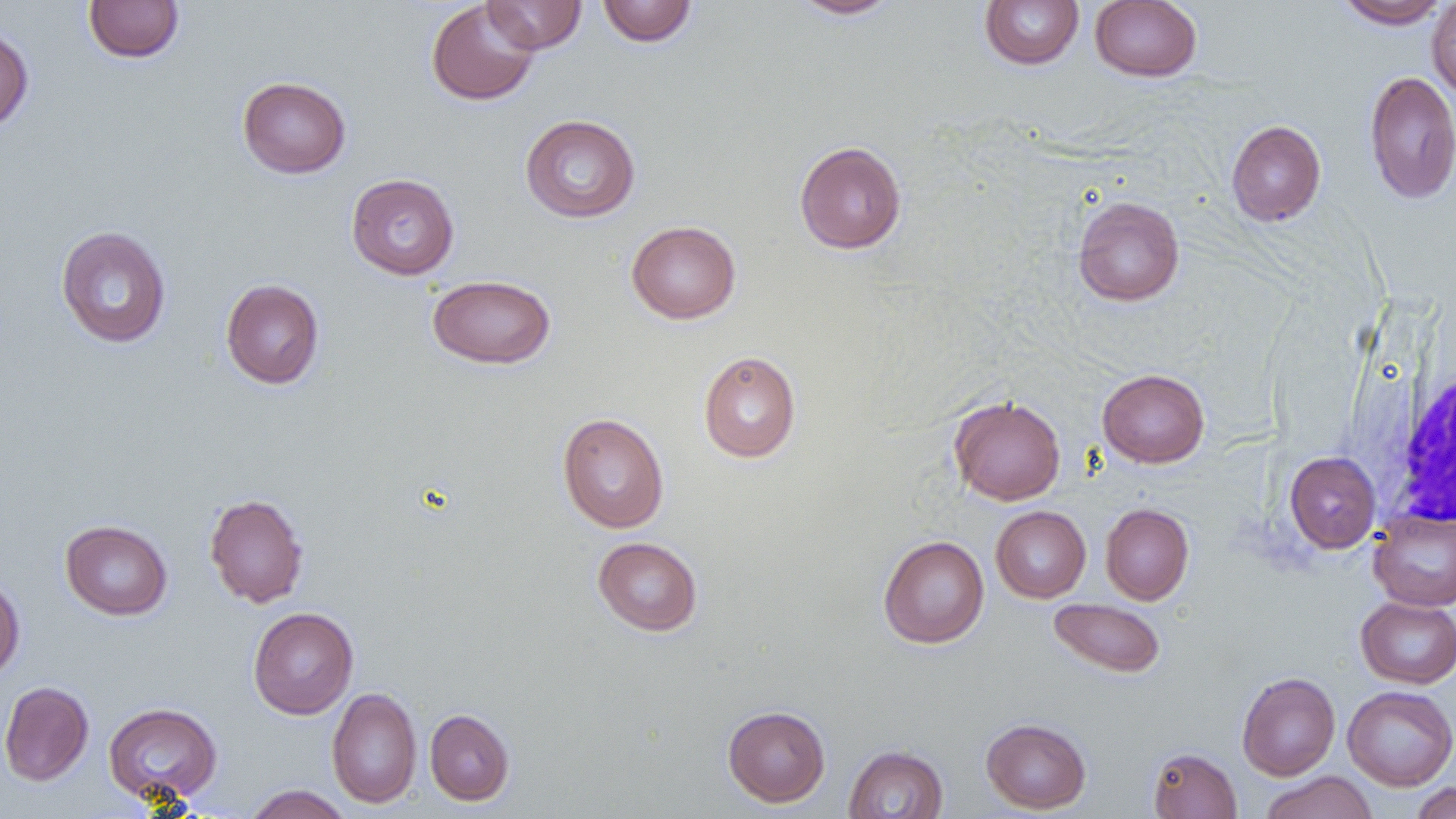
Approximate bounding boxes as (x1,y1)-(x2,y2) corner pairs in pixels. Uninfected red blood cell locations: (83,0)-(184,63), (426,0)-(540,106), (482,0)-(587,54), (788,0)-(902,20), (979,0)-(1084,69), (1334,0)-(1451,29), (1426,0)-(1456,103), (597,1)-(698,46), (1089,1)-(1202,82), (0,25)-(34,134), (1364,71)-(1456,205), (237,76)-(351,178), (520,114)-(640,223), (1226,120)-(1326,226), (794,141)-(906,254), (346,173)-(459,280), (1072,196)-(1185,306), (626,220)-(741,324), (55,226)-(171,348), (426,274)-(556,369), (220,278)-(325,389), (698,351)-(801,463), (1097,368)-(1210,467), (948,395)-(1066,505), (557,412)-(669,533), (1284,451)-(1381,553), (204,493)-(309,608), (1100,503)-(1194,605), (990,506)-(1091,603), (1369,510)-(1456,611), (60,519)-(173,620), (878,535)-(989,648), (592,536)-(703,636), (0,575)-(25,680), (1355,596)-(1456,688), (1048,598)-(1166,678), (248,607)-(359,719), (1236,671)-(1340,780), (0,680)-(94,786), (1342,685)-(1456,790), (326,686)-(422,808), (103,702)-(222,805), (722,705)-(830,807), (424,708)-(515,806), (981,717)-(1092,814), (843,745)-(949,818), (1147,747)-(1242,818), (1260,771)-(1377,819), (1409,782)-(1456,819), (243,785)-(353,819). White blood cell locations: (1390,362)-(1456,530). Slide-level diagnosis: no evidence of blood parasites. Single field of view. Optical microscopy. Captured at 1000x magnification. Image is 1456×819 pixels. Thin blood smear.